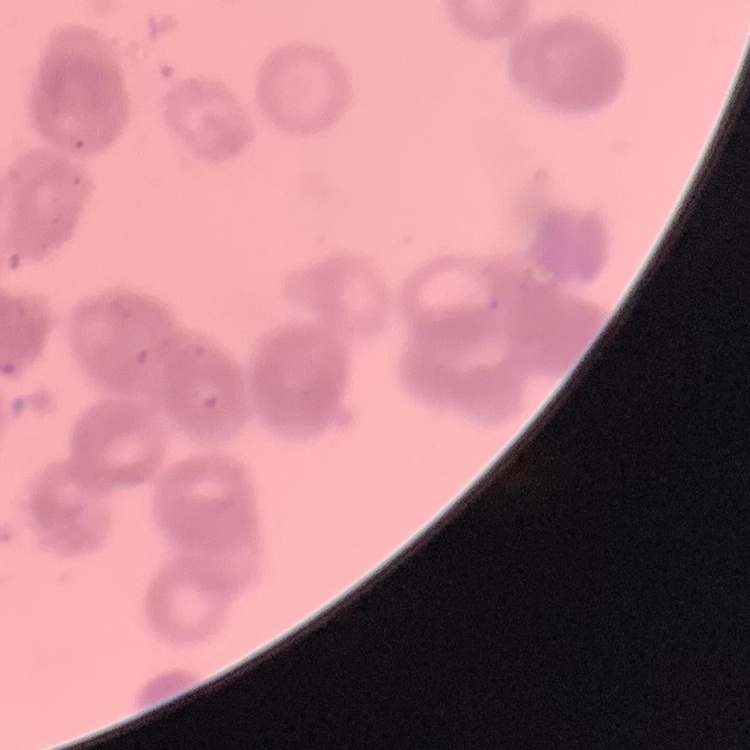 The red blood cells exhibit rouleaux formation. One tile cut from a larger photomicrograph. Thin blood film. Stained with either Field's or Giemsa.